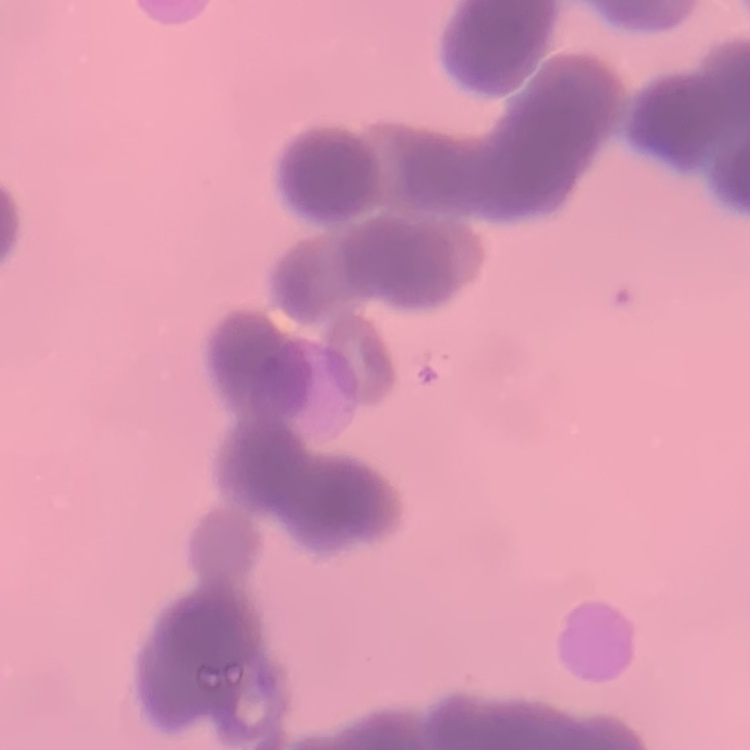
erythrocyte morphology = rouleaux formation
stain = Field's or Giemsa
preparation = thin blood film
image type = square crop of a larger photomicrograph